Find each parasitized red blood cell.
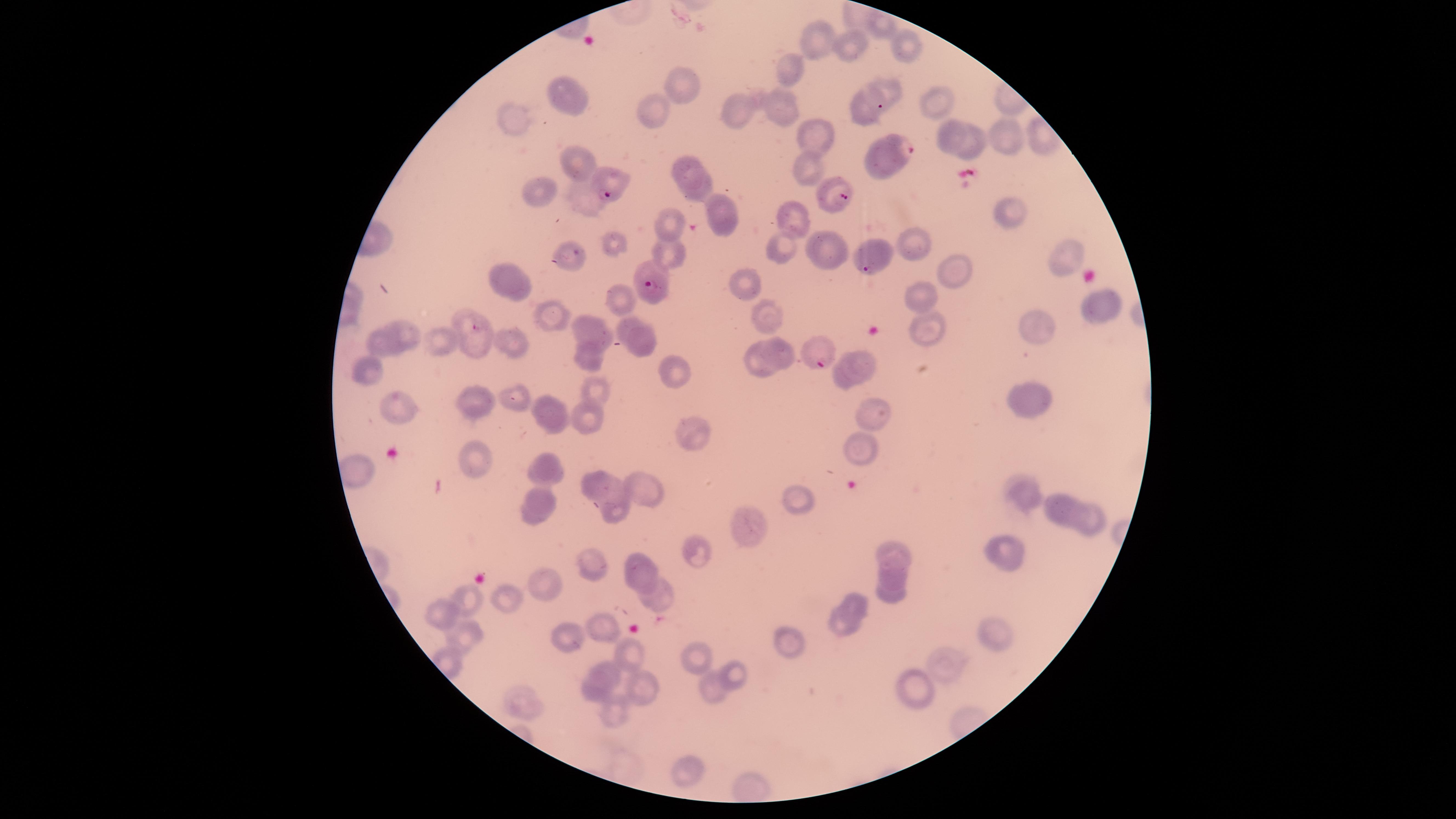

Approximate marker points, in pixels from the top-left corner.
Parasitized red blood cells: (x=898, y=149), (x=608, y=180), (x=837, y=196), (x=873, y=255), (x=656, y=290), (x=812, y=356).

image_size: 1456×819 pixels
species: Plasmodium falciparum
field_of_view: single
visible_region: circular
uninfected_red_blood_cells: 'approximate marker points, in pixels from the top-left corner: (x=812, y=42), (x=843, y=44), (x=903, y=49), (x=789, y=63), (x=678, y=83), (x=891, y=87), (x=571, y=97), (x=935, y=102), (x=855, y=104), (x=735, y=106), (x=781, y=106), (x=651, y=107), (x=510, y=114), (x=809, y=137), (x=954, y=138), (x=1008, y=138), (x=978, y=143), (x=581, y=158), (x=689, y=162), (x=809, y=163), (x=541, y=186), (x=695, y=189), (x=725, y=213), (x=1002, y=214), (x=793, y=215), (x=671, y=222), (x=787, y=244), (x=915, y=244), (x=616, y=247), (x=827, y=247), (x=674, y=253), (x=1056, y=254), (x=564, y=261), (x=946, y=269), (x=503, y=270), (x=747, y=285), (x=520, y=291), (x=619, y=295), (x=919, y=300), (x=1113, y=300), (x=768, y=307), (x=1088, y=312), (x=552, y=318), (x=465, y=320), (x=625, y=322), (x=1033, y=325), (x=405, y=329), (x=595, y=332), (x=929, y=333), (x=643, y=341), (x=513, y=342), (x=380, y=343), (x=440, y=343), (x=474, y=347), (x=779, y=347), (x=592, y=357), (x=863, y=363), (x=757, y=365), (x=675, y=370), (x=369, y=374), (x=840, y=379), (x=597, y=388), (x=517, y=398), (x=1031, y=398), (x=474, y=399), (x=392, y=407), (x=875, y=411), (x=550, y=412), (x=588, y=419), (x=689, y=429), (x=862, y=447), (x=469, y=455), (x=542, y=469), (x=597, y=483), (x=647, y=485), (x=799, y=498), (x=1025, y=498), (x=538, y=504), (x=1050, y=506), (x=615, y=512), (x=1069, y=513), (x=1086, y=519), (x=742, y=527), (x=899, y=551), (x=1007, y=551), (x=699, y=553), (x=595, y=561), (x=638, y=567), (x=893, y=578), (x=546, y=584), (x=655, y=595), (x=892, y=596), (x=509, y=598), (x=471, y=600), (x=854, y=601), (x=444, y=612), (x=841, y=625), (x=604, y=626), (x=465, y=631), (x=995, y=631), (x=573, y=632), (x=794, y=641), (x=697, y=653), (x=629, y=655), (x=946, y=667), (x=607, y=674), (x=740, y=674), (x=712, y=684), (x=911, y=686), (x=641, y=687), (x=592, y=694), (x=523, y=701), (x=616, y=713), (x=688, y=767)'
preparation: thin blood smear
capture: smartphone photograph through the microscope eyepiece
stain: Giemsa